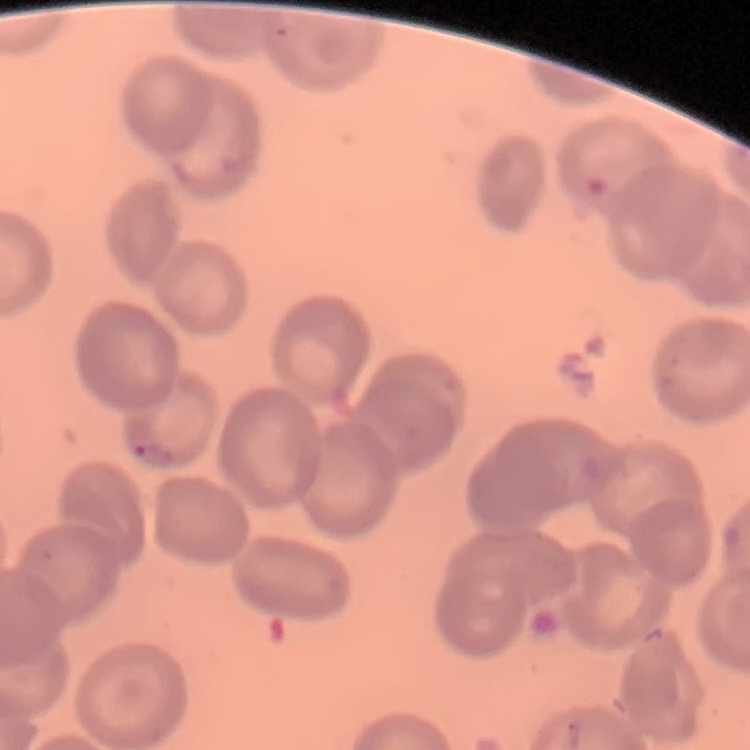 The erythrocytes show no rouleaux formation. Thin peripheral smear. Field's or Giemsa stain. One tile cut from a larger photomicrograph.